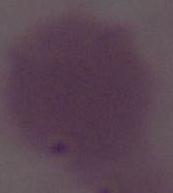

Micrograph. 1000x magnification. A red blood cell is seen.